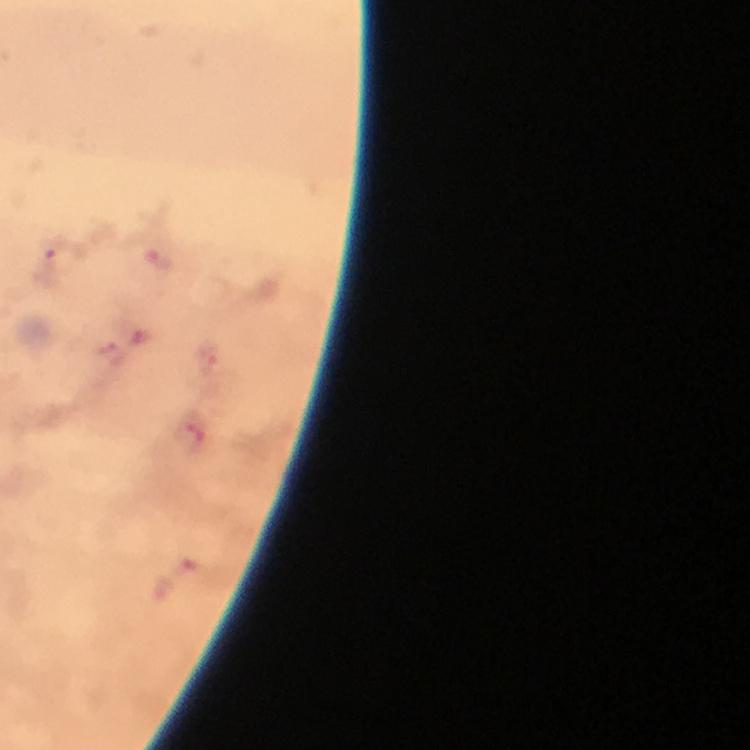
Approximate centers as {x, y} in pixels. Malaria parasite locations: {157, 259}, {51, 264}, {208, 360}, {158, 586}. 100x magnification. Immersion oil was used. A crop from one field of view. Giemsa-stained preparation. From a diagnostic examination for malaria. Smartphone photograph taken through a microscope. Thick blood smear. Image is 750×750 pixels.